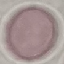
Summary:
  - Result: no malaria parasites seen
  - Capture: smartphone camera at the microscope eyepiece
  - Image type: cell patch, automatically extracted from a larger field of view and resized to 64 × 64 pixels
  - Preparation: thin blood film
  - Stain: Giemsa